Report the malaria status of this cell.
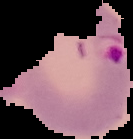

It is parasitized.

image size = 133×139 pixels
preparation = thin blood smear
image type = cell region segmented out of the field of view; surrounding area masked to black